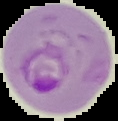
preparation = thin blood smear
result = Plasmodium parasites detected
image size = 118×121 pixels
image type = segmented cell region on a black background